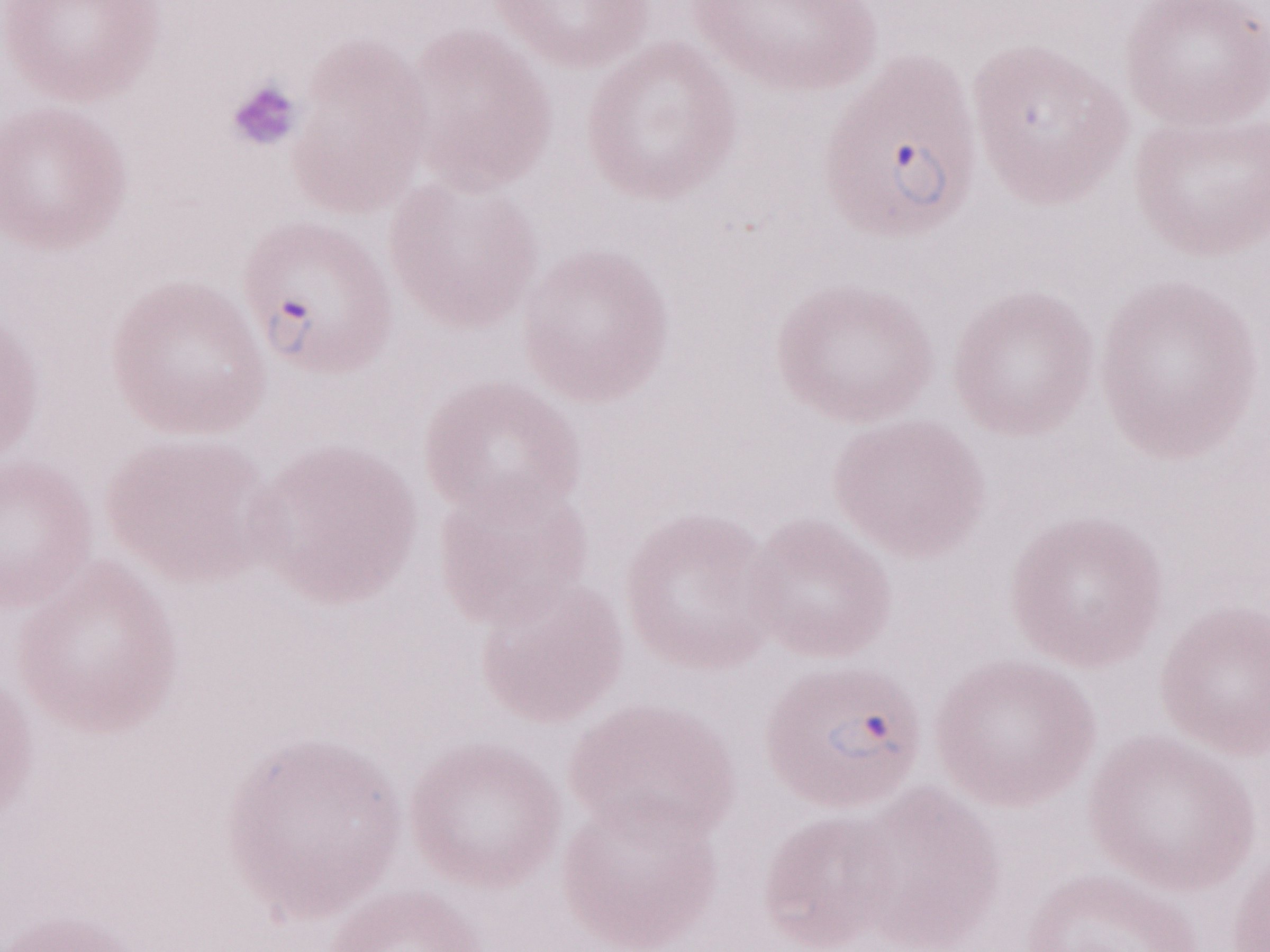
Patient-level malaria diagnosis: positive. Image is 1270×952 pixels. Thin peripheral-blood smear. May-Grünwald-Giemsa stain. Olympus BX43 microscope, Olympus DP73 camera. 1,000x magnification. Single field of view.